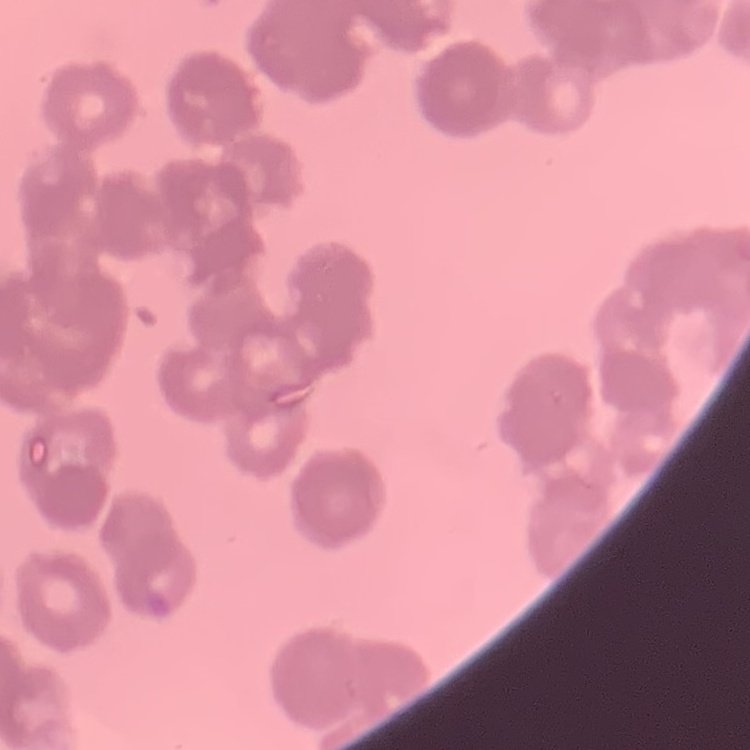

The erythrocytes exhibit rouleaux formation. One tile cut from a larger photomicrograph. Stained with either Field's or Giemsa. Thin peripheral smear.